Classify this cell by malaria status.
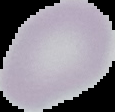

It is uninfected.

Summary:
  - Image type: cell region segmented out of the field of view; surrounding area masked to black
  - Preparation: thin blood film
  - Image size: 115×112 pixels